Give the preparation type.
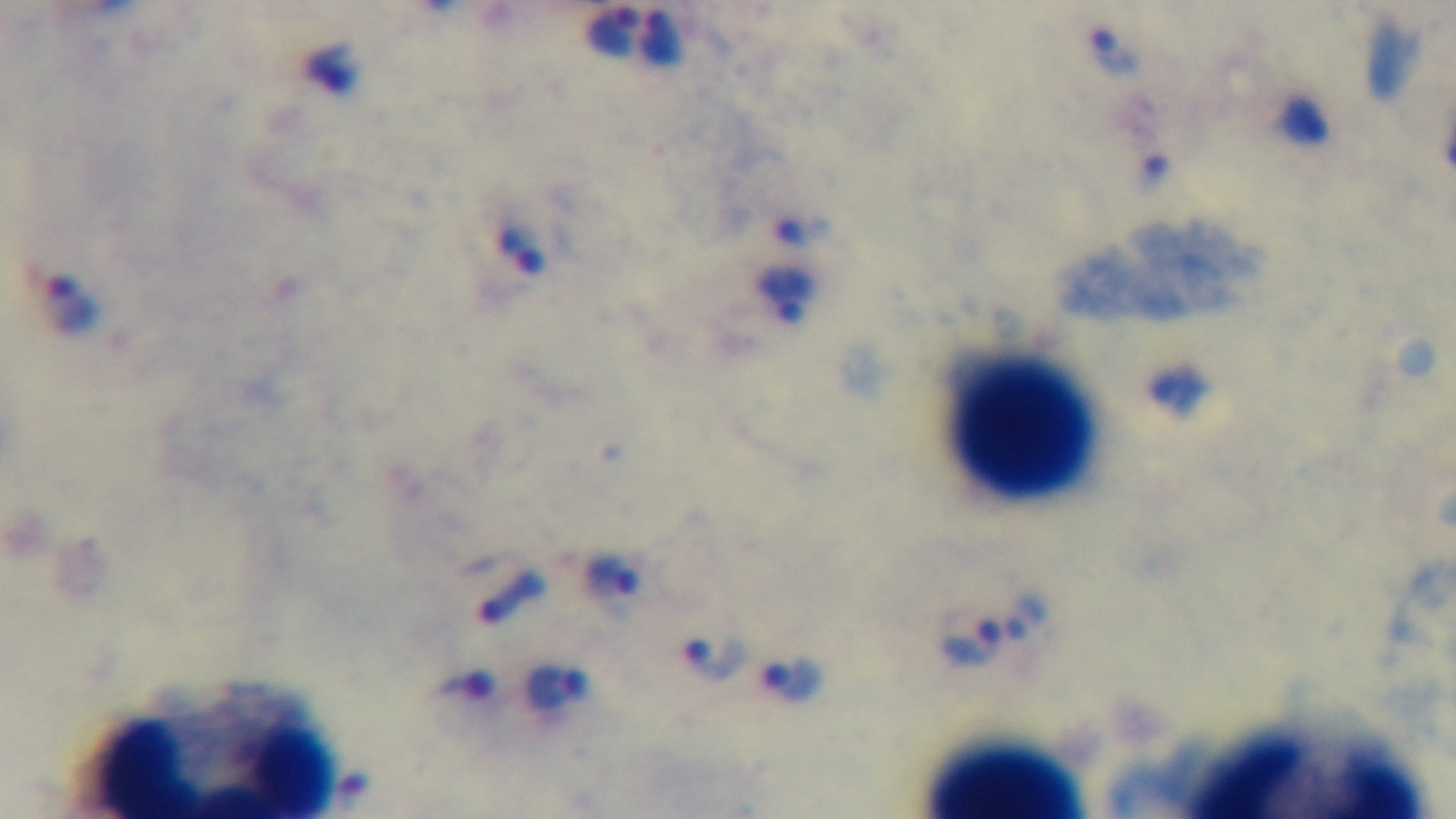

It is a thick blood film.

{
  "modality": "light microscopy",
  "field_of_view": "single",
  "stain": "Giemsa",
  "malaria_status": "positive",
  "capture": "mounted 4K digital camera",
  "objective": "100x oil immersion"
}